Classify this cell by malaria status.
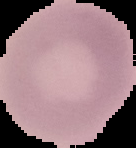

Uninfected.

{
  "image_size": "136×148 pixels",
  "preparation": "thin blood smear",
  "image_type": "segmented cell region on a black background"
}